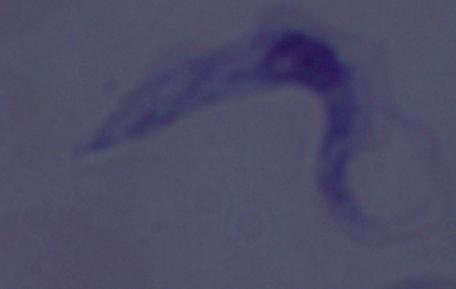
identification = trypanosome
modality = micrograph
magnification = 1000x